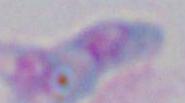 Captured at 1000x magnification. Photomicrograph. Toxoplasma gondii is seen.